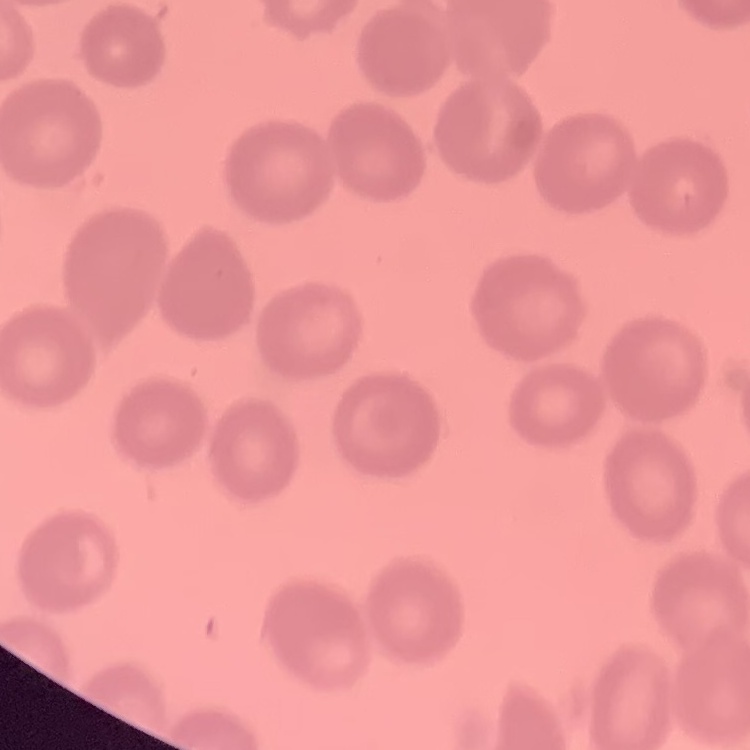
Summary:
  - Erythrocyte morphology: no rouleaux formation
  - Stain: Field's or Giemsa
  - Image type: one tile cut from a larger photomicrograph
  - Preparation: thin blood smear